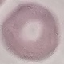

Summary:
  - Result: no malaria parasites seen
  - Stain: Giemsa
  - Capture: smartphone camera at the microscope eyepiece
  - Image type: cell patch, automatically extracted from a larger field of view and resized to 64 × 64 pixels
  - Preparation: thin blood smear